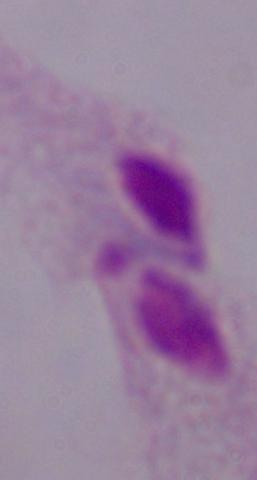
A trichomonad is shown. 1000x magnification. Micrograph.